Name the parasite shown.
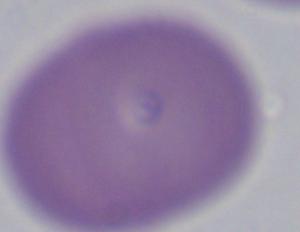

This is Babesia.

Summary:
  - Magnification: 1000x
  - Modality: photomicrograph